Give the preparation type.
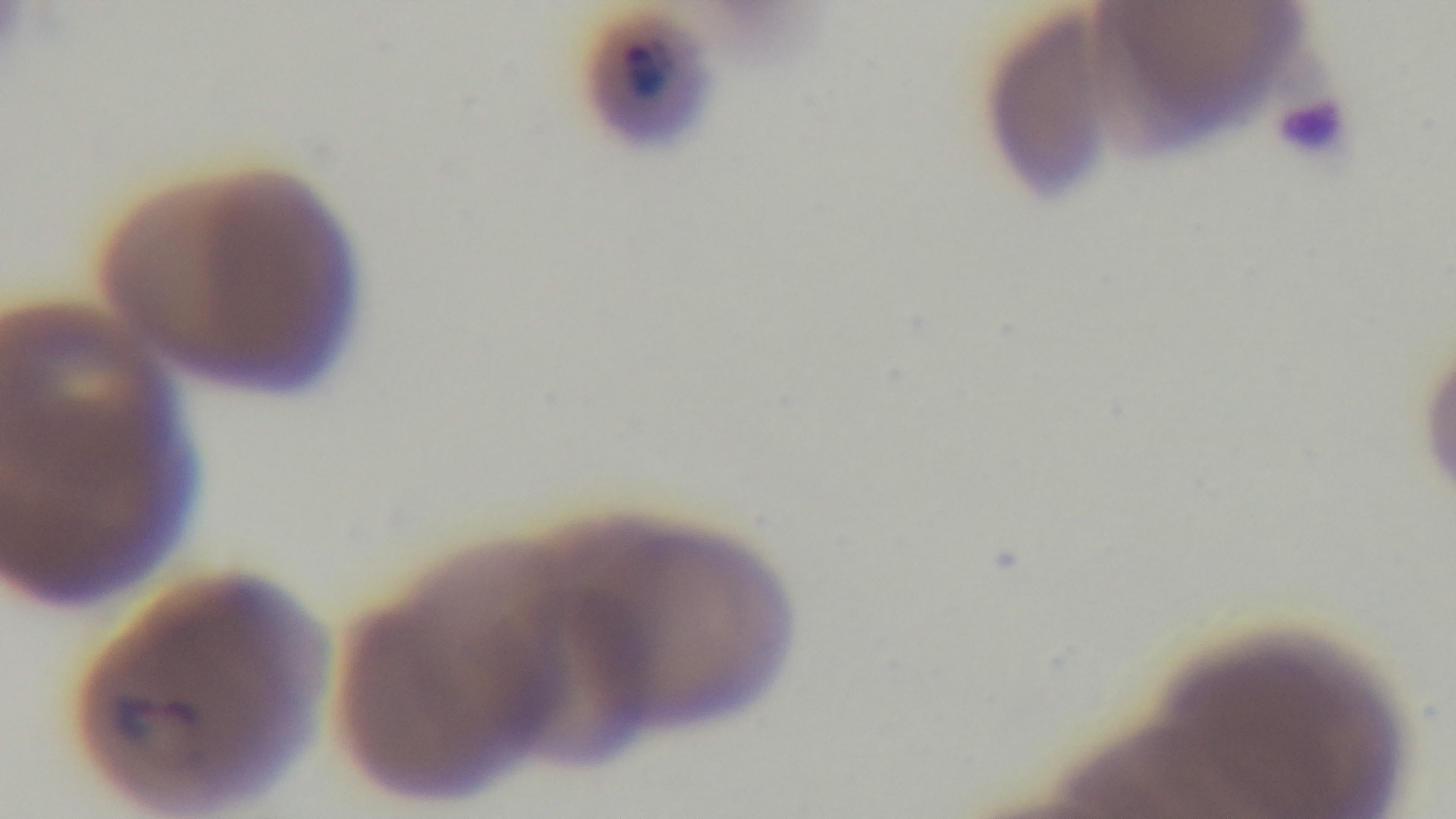
A thin smear.

{
  "stain": "Giemsa",
  "capture": "mounted 4K digital camera",
  "field_of_view": "single",
  "objective": "100x oil immersion",
  "modality": "light microscopy",
  "malaria_status": "positive"
}